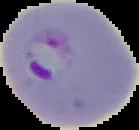

The area outside the segmented cell region is set to black. Malaria status: parasitized. From a thin blood smear. Image is 139×130 pixels.